Name the blood parasite species.
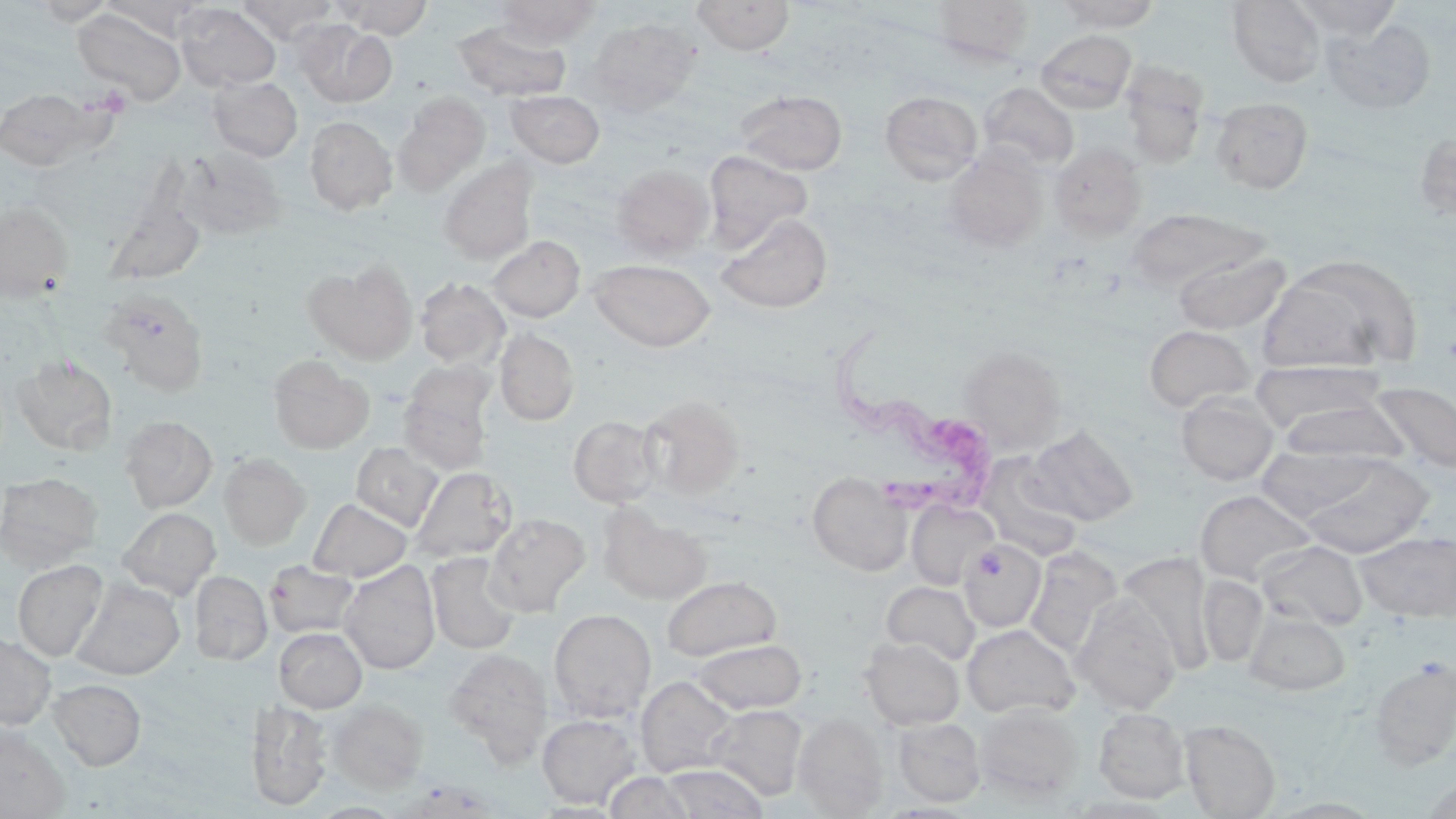
Trypanosoma brucei.

Approximate bounding boxes as (x1, y1, x2, y2) in pixels. Trypanosoma brucei locations: (824, 326, 995, 521). Uninfected red blood cell locations: (32, 0, 117, 25), (336, 0, 433, 39), (494, 0, 601, 49), (691, 0, 796, 55), (930, 0, 1035, 65), (1054, 0, 1162, 31), (1227, 0, 1326, 88), (1293, 0, 1403, 41), (104, 1, 212, 42), (238, 1, 339, 43), (175, 3, 281, 91), (73, 8, 186, 105), (586, 17, 701, 116), (1323, 18, 1436, 114), (292, 20, 397, 107), (453, 20, 572, 102), (1035, 29, 1136, 114), (1119, 61, 1210, 167), (208, 75, 302, 162), (978, 82, 1079, 171), (0, 88, 110, 171), (506, 90, 605, 168), (735, 90, 848, 174), (880, 91, 983, 184), (393, 92, 489, 195), (1210, 96, 1313, 194), (304, 116, 398, 214), (1413, 129, 1456, 226), (1049, 143, 1147, 239), (177, 146, 285, 240), (941, 148, 1048, 251), (703, 150, 813, 252), (438, 160, 538, 265), (610, 163, 716, 262), (103, 194, 207, 287), (0, 201, 74, 302), (1126, 206, 1267, 293), (716, 212, 832, 313), (486, 235, 585, 322), (1172, 248, 1291, 333), (1260, 254, 1423, 375), (589, 258, 716, 352), (304, 261, 417, 363), (415, 277, 510, 369), (99, 287, 209, 395), (1143, 324, 1256, 413), (494, 328, 580, 426), (958, 345, 1066, 453), (12, 354, 118, 455), (268, 354, 374, 453), (1250, 359, 1388, 433), (398, 372, 495, 475), (1370, 381, 1456, 475), (1176, 390, 1279, 485), (638, 395, 745, 500), (1276, 400, 1410, 464), (569, 415, 662, 507), (120, 416, 218, 512), (1026, 424, 1139, 526), (351, 442, 444, 531), (1256, 444, 1379, 520), (219, 454, 311, 549), (977, 454, 1082, 560), (1298, 454, 1433, 558), (411, 466, 516, 562), (0, 472, 102, 571), (807, 472, 912, 576), (1195, 488, 1316, 585), (308, 498, 412, 582), (906, 500, 998, 590), (599, 505, 712, 605), (117, 507, 221, 600), (483, 513, 591, 616), (1356, 531, 1455, 622), (959, 538, 1046, 632), (1256, 540, 1368, 630), (1024, 547, 1122, 659), (426, 552, 520, 655), (1116, 552, 1217, 674), (13, 559, 107, 661), (265, 561, 361, 638), (339, 562, 440, 674), (189, 570, 272, 664), (1198, 573, 1268, 667), (661, 575, 782, 661), (71, 579, 186, 680), (881, 580, 980, 664), (1071, 595, 1181, 714), (549, 609, 656, 722), (1245, 611, 1350, 695), (962, 624, 1080, 719), (274, 627, 367, 712), (0, 634, 55, 730), (861, 637, 965, 730), (690, 638, 807, 714), (443, 648, 553, 765), (1369, 658, 1456, 770), (636, 676, 739, 779), (49, 678, 146, 769), (329, 699, 427, 792), (246, 700, 330, 810), (975, 702, 1084, 802), (707, 705, 806, 801), (1094, 707, 1191, 802), (794, 712, 888, 817), (537, 714, 640, 807), (894, 717, 986, 807), (1180, 719, 1281, 818), (0, 725, 70, 818), (661, 763, 768, 818), (603, 771, 696, 818). Image is 1456×819 pixels. One field of a larger specimen. May-Grünwald-Giemsa stain. Optical microscopy. Thin blood smear. 1000x magnification.